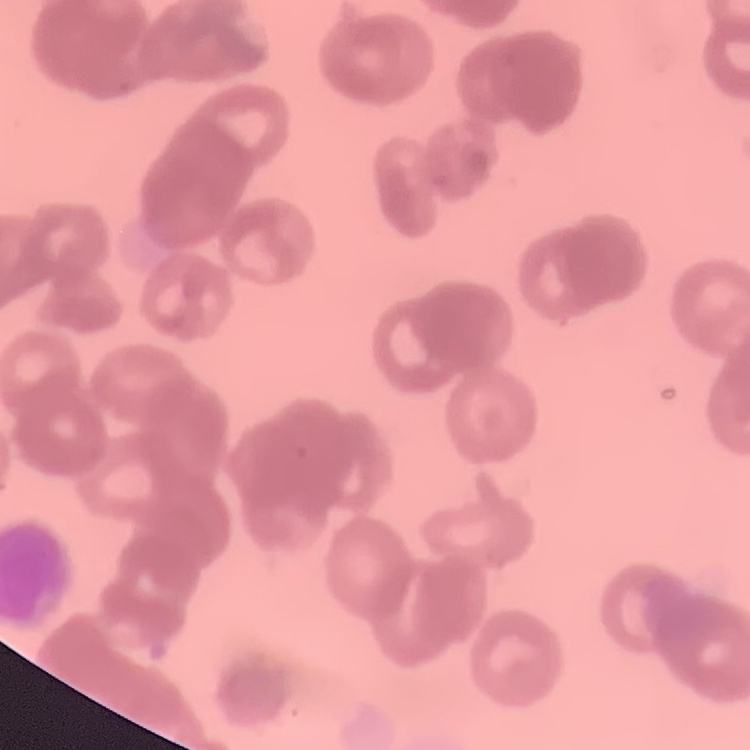
red blood cell morphology = rouleaux formation
preparation = thin peripheral smear
image type = one tile cut from a larger photomicrograph
stain = Field's or Giemsa